Classify this cell by malaria status.
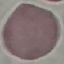

Uninfected.

image_type: cell patch, automatically extracted from a larger field of view and resized to 64 × 64 pixels
capture: smartphone through the microscope eyepiece
preparation: thin blood smear
stain: Giemsa